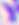 Photomicrograph. 400x magnification. Toxoplasma gondii is seen.